Assess this cell for malaria.
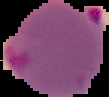

Parasitized.

image type = segmented cell region with the area outside set to black
preparation = thin blood film
image size = 109×97 pixels